Name the parasite shown.
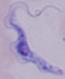

This is a trypanosome.

magnification: 1000x
modality: photomicrograph